Identify the parasite.
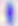
This is Toxoplasma gondii.

Captured at 400x magnification. Micrograph.